Point out each malaria parasite.
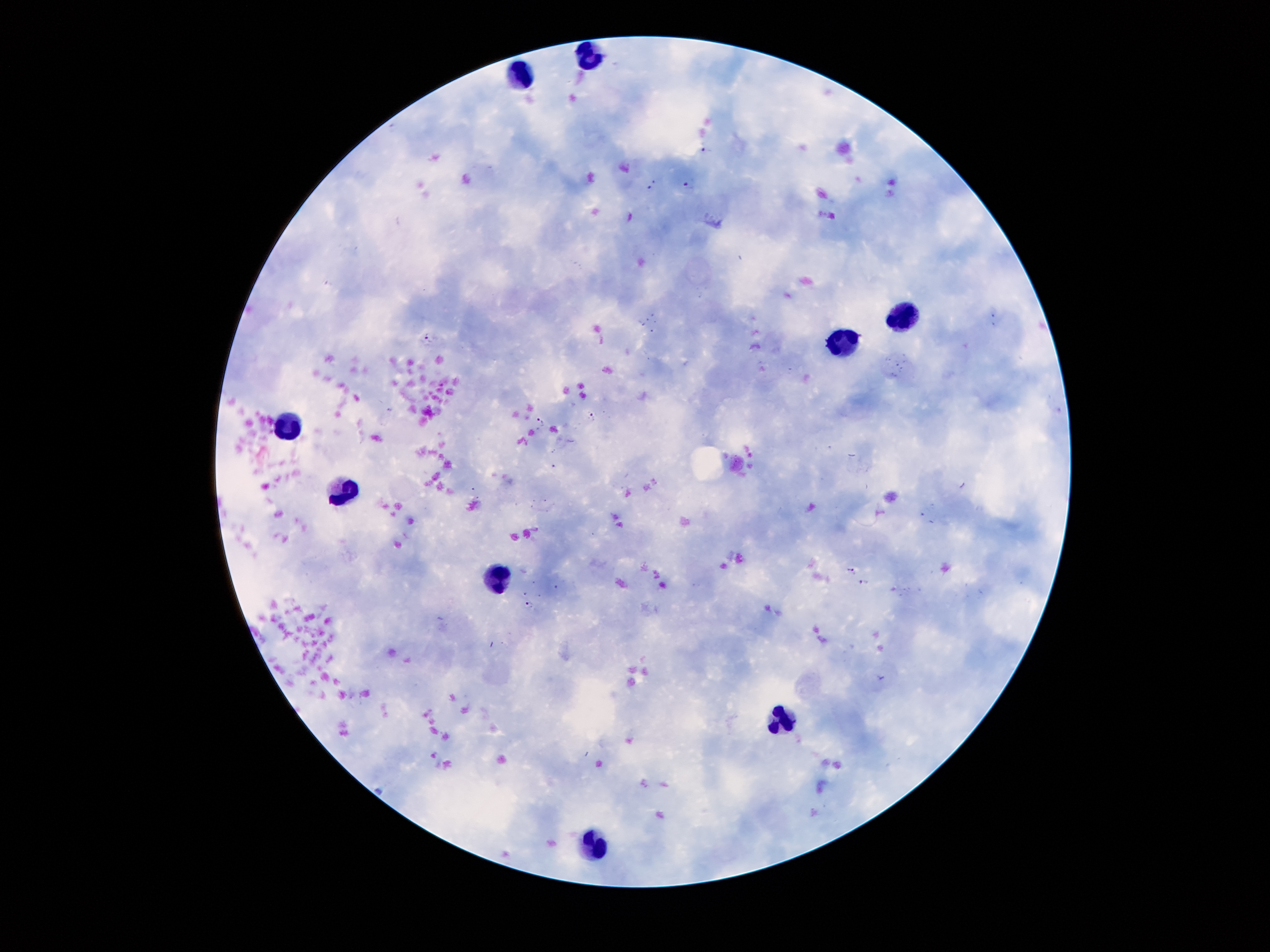
Approximate centers as (x, y) in pixels.
Malaria parasites: (708, 151), (651, 186), (688, 186), (430, 338), (592, 416), (541, 421), (851, 572), (867, 584), (528, 603).

Summary:
  - Leukocyte locations: (588, 54), (524, 75), (896, 319), (841, 346), (288, 425), (337, 486), (496, 576), (785, 717), (593, 845)
  - Patient malaria status: infected with Plasmodium falciparum
  - Image size: 1270×952 pixels
  - Capture: smartphone camera through the microscope eyepiece
  - Preparation: thick peripheral-blood smear
  - Stain: Giemsa
  - Magnification: 100x
  - Field of view: single